Locate every Plasmodium parasite.
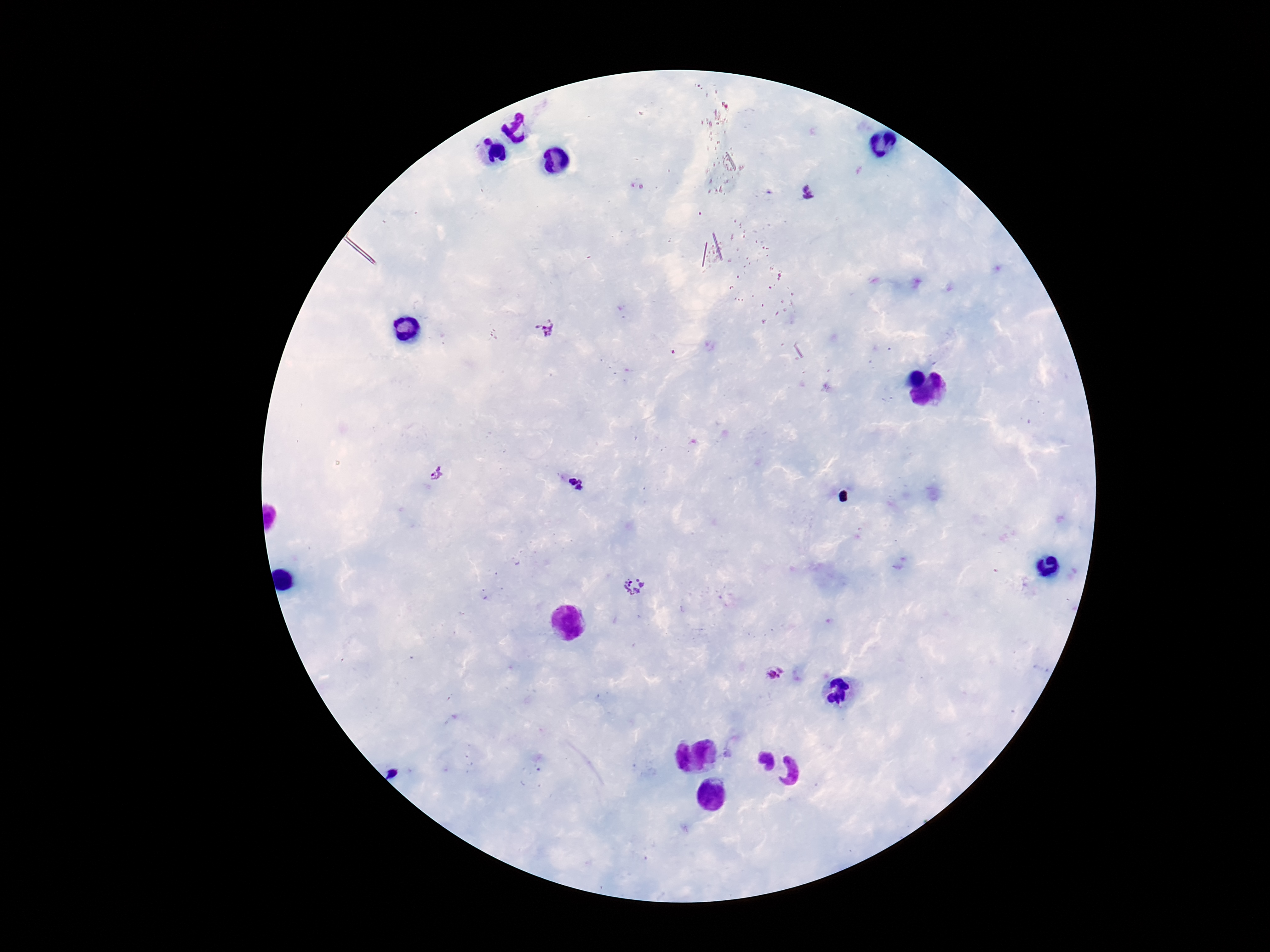

Approximate centers as [x, y] in pixels.
Plasmodium parasites: [808, 194], [544, 329], [438, 473], [577, 484], [634, 588], [775, 675].

magnification: 100x
preparation: thick peripheral-blood smear
capture: smartphone camera through the microscope eyepiece
field_of_view: single
image_size: 1270×952 pixels
stain: Giemsa
patient_malaria_status: infected